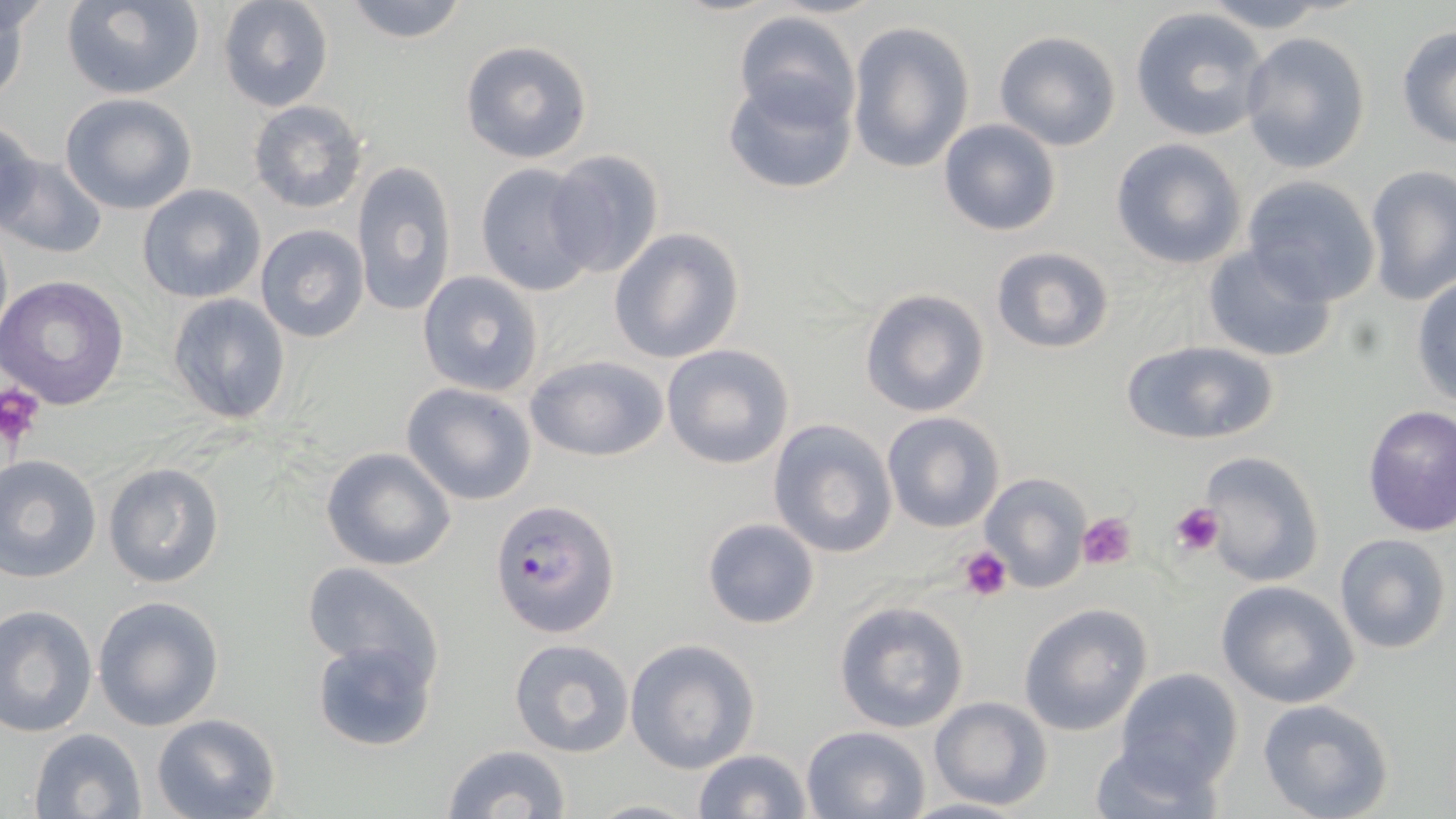
slide-level diagnosis = Plasmodium falciparum
platelet locations = approximate bounding boxes as [x1, y1, x2, y2] in pixels: [0, 384, 46, 452], [1170, 501, 1224, 555], [1078, 511, 1136, 572], [958, 548, 1011, 602]
preparation = thin blood film
image size = 1456×819 pixels
magnification = 1000x
modality = light microscopy
field of view = single
Plasmodium falciparum-infected red blood cell locations = approximate bounding boxes as [x1, y1, x2, y2] in pixels: [491, 497, 620, 639]
stain = May-Grünwald-Giemsa
uninfected red blood cell locations = approximate bounding boxes as [x1, y1, x2, y2] in pixels: [60, 0, 204, 99], [339, 0, 472, 44], [1196, 0, 1342, 30], [0, 1, 29, 112], [218, 1, 334, 111], [1130, 7, 1272, 143], [731, 10, 861, 129], [847, 19, 975, 174], [1395, 26, 1456, 150], [994, 30, 1123, 151], [1238, 30, 1373, 174], [460, 39, 593, 164], [722, 73, 856, 197], [59, 93, 197, 214], [247, 98, 368, 213], [2, 119, 42, 236], [938, 119, 1063, 237], [1110, 138, 1246, 270], [546, 149, 665, 279], [4, 155, 107, 260], [351, 160, 457, 318], [475, 162, 597, 296], [1364, 167, 1455, 305], [1241, 176, 1382, 305], [138, 183, 265, 303], [255, 224, 368, 343], [610, 227, 745, 364], [1202, 243, 1339, 362], [990, 246, 1116, 354], [416, 270, 544, 396], [0, 274, 130, 410], [1411, 275, 1456, 409], [860, 287, 990, 417], [167, 294, 291, 425], [1120, 338, 1281, 446], [661, 343, 795, 470], [523, 354, 670, 461], [400, 382, 538, 506], [1361, 404, 1456, 536], [880, 410, 1006, 533], [766, 418, 898, 559], [321, 448, 458, 570], [1200, 452, 1324, 589], [0, 455, 102, 582], [104, 461, 225, 588], [979, 471, 1092, 593], [701, 517, 821, 630], [1333, 533, 1452, 655], [301, 561, 442, 682], [1215, 581, 1359, 708], [92, 596, 224, 731], [833, 600, 970, 733], [0, 604, 98, 737], [1017, 604, 1152, 736], [309, 635, 439, 751], [507, 638, 636, 757], [626, 639, 760, 773], [1112, 668, 1245, 790], [927, 696, 1054, 807], [1257, 698, 1396, 819], [150, 713, 281, 819], [800, 724, 931, 817], [26, 728, 149, 818], [1088, 736, 1225, 818], [439, 744, 572, 819], [691, 749, 813, 819], [900, 796, 1030, 818], [586, 797, 704, 818]